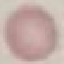
result = no malaria parasites detected
stain = Giemsa
capture = smartphone through the microscope eyepiece
image type = cell patch, automatically extracted from a larger field of view and resized to 64 × 64 pixels
preparation = thin smear